Name the cell type shown.
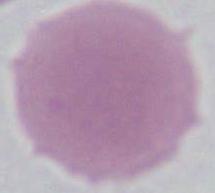
An erythrocyte.

Micrograph. Captured at 1000x magnification.